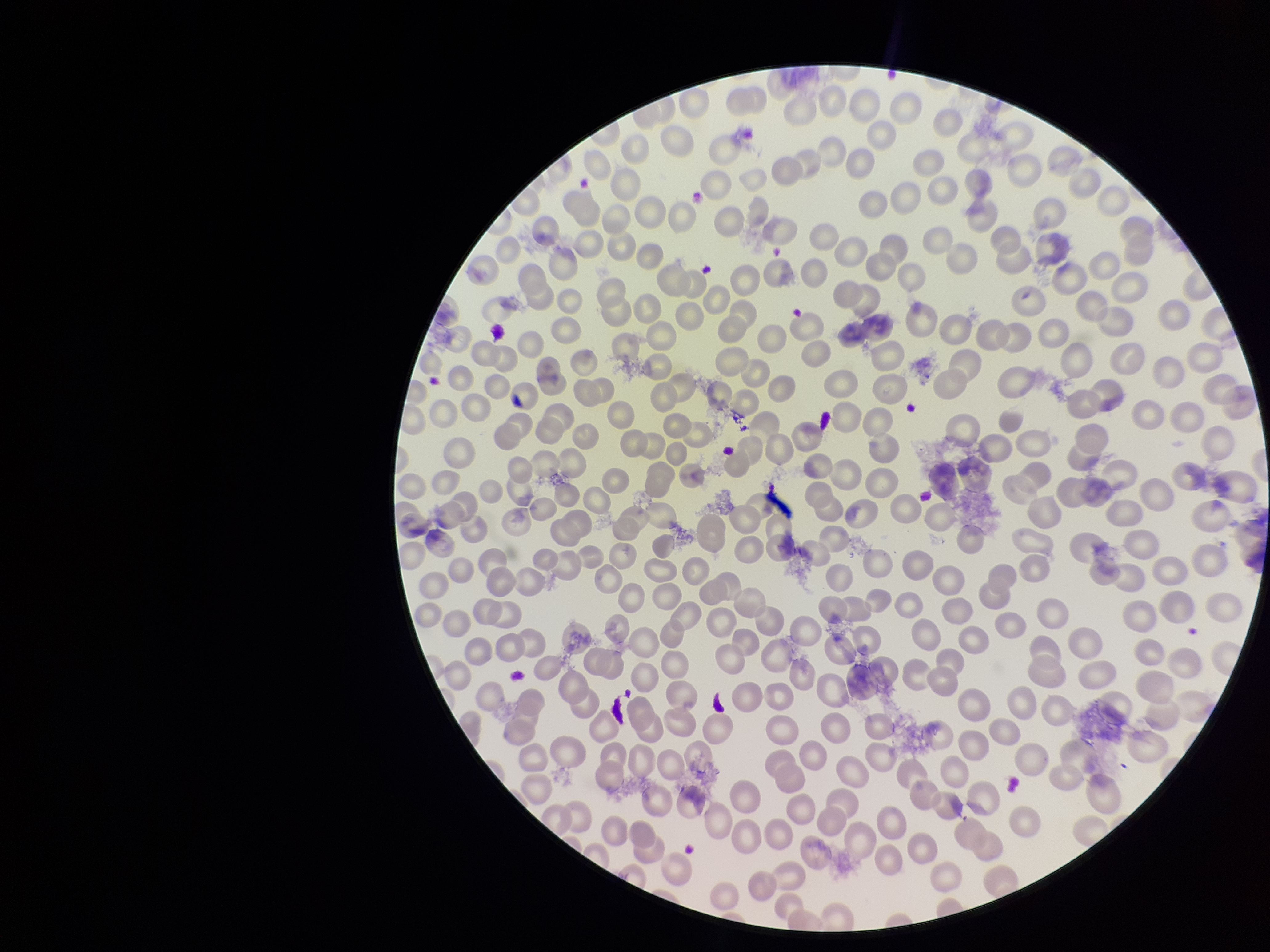

Summary:
  - Preparation: thin smear
  - Image size: 1270×952 pixels
  - Parasitized red blood cell count: 0
  - Patient malaria status: positive
  - Capture: smartphone photograph through the microscope eyepiece
  - Stain: Giemsa
  - Parasitized red blood cells: none seen
  - Species reported for this patient: Plasmodium vivax
  - Red blood cell count: 318
  - Field of view: one from this slide